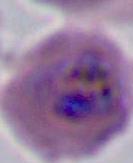

Summary:
  - Magnification: 400x or 1000x
  - Modality: micrograph
  - Identification: Plasmodium